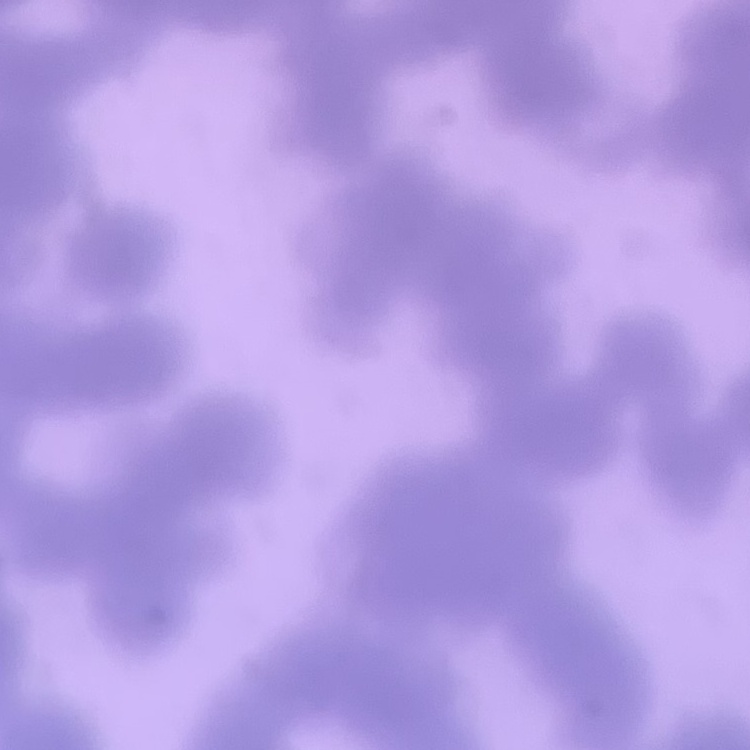

red blood cell morphology = rouleaux formation
preparation = thin blood film
image type = one tile cut from a larger photomicrograph
stain = Field's or Giemsa